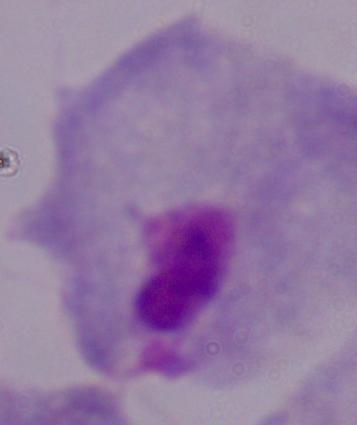
{
  "modality": "photomicrograph",
  "magnification": "1000x",
  "identification": "trichomonad"
}